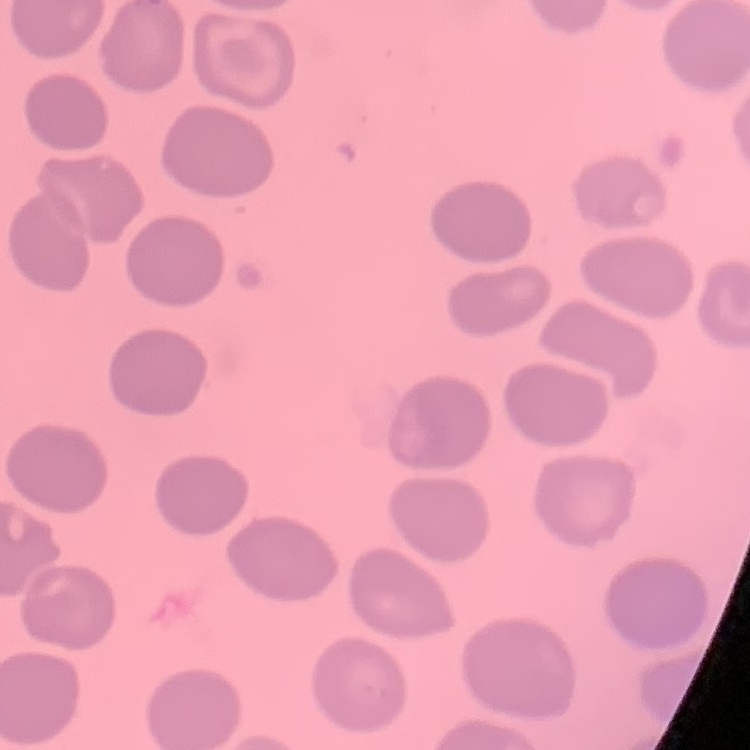 The red blood cells exhibit no rouleaux formation. Thin blood smear. One tile cut from a larger photomicrograph. Field's or Giemsa stain.